Name the blood parasite species.
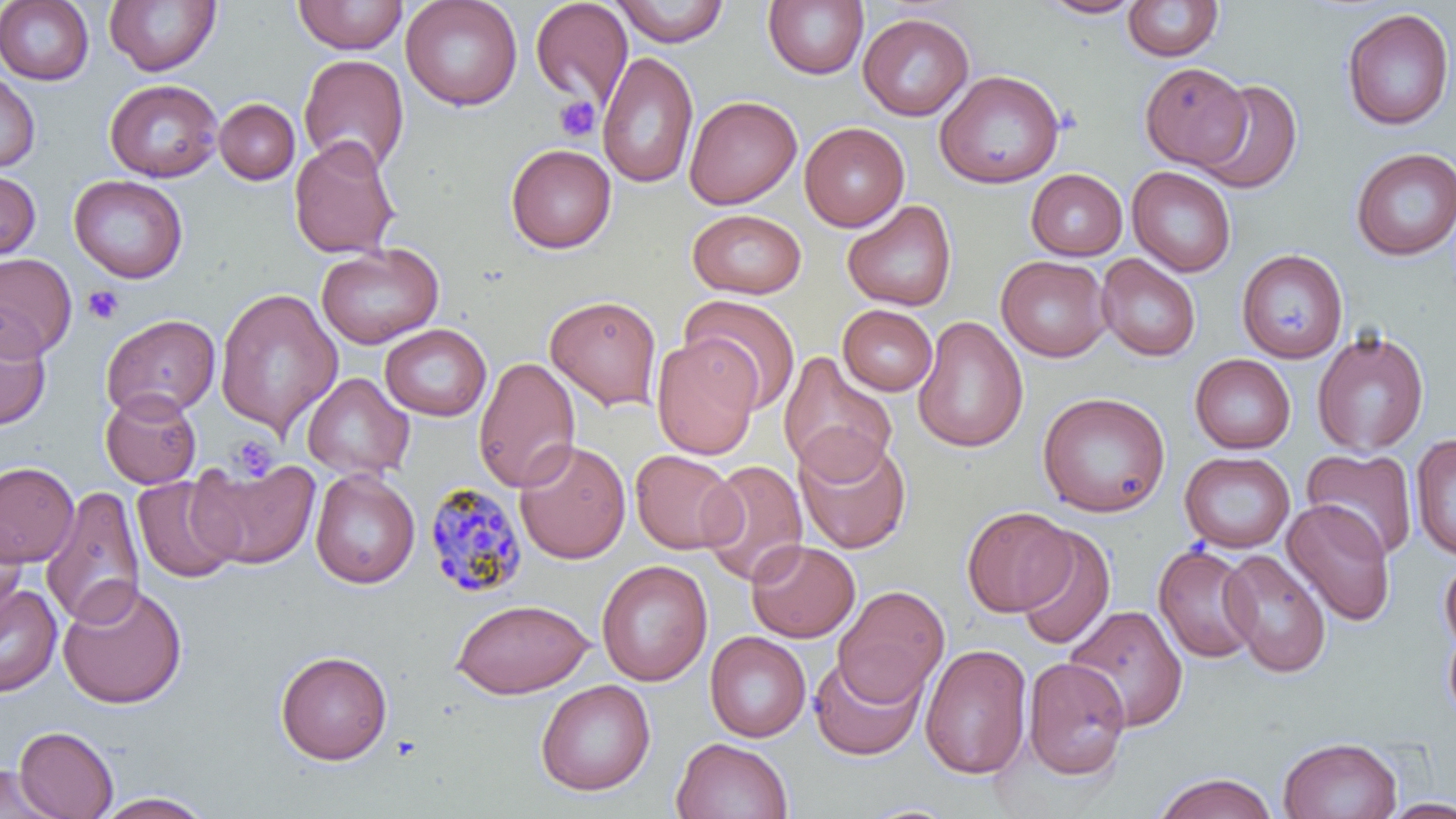
Plasmodium malariae.

Approximate bounding boxes as (x1,y1)-(x2,y2) corner pairs in pixels. Plasmodium malariae-infected red blood cell locations: (423,482)-(530,599). Platelet locations: (554,96)-(601,143), (82,285)-(124,326), (228,434)-(279,481). Uninfected red blood cell locations: (0,0)-(94,85), (292,0)-(409,54), (401,0)-(523,111), (530,0)-(633,108), (611,0)-(730,47), (1035,0)-(1146,19), (104,1)-(222,76), (763,1)-(869,80), (1122,1)-(1222,62), (1340,8)-(1454,131), (858,12)-(974,120), (597,51)-(699,188), (298,54)-(410,174), (1140,62)-(1251,168), (935,69)-(1065,189), (0,70)-(40,172), (104,79)-(222,182), (1196,79)-(1303,194), (684,95)-(802,209), (214,99)-(299,185), (799,123)-(909,231), (288,135)-(401,259), (505,144)-(617,253), (1351,148)-(1456,260), (1127,165)-(1236,277), (0,168)-(40,262), (1026,169)-(1127,260), (69,174)-(187,283), (841,199)-(957,312), (687,209)-(807,299), (316,243)-(443,349), (1236,249)-(1348,363), (0,253)-(77,360), (1096,253)-(1201,362), (996,255)-(1111,362), (215,288)-(341,435), (545,294)-(662,410), (681,295)-(802,412), (837,304)-(938,396), (101,313)-(220,420), (0,315)-(52,431), (912,316)-(1028,454), (380,324)-(492,420), (1312,329)-(1430,456), (651,335)-(761,460), (777,351)-(898,481), (1189,353)-(1296,454), (473,356)-(580,492), (301,372)-(415,482), (101,389)-(202,488), (1036,391)-(1171,518), (793,432)-(911,555), (1410,435)-(1456,560), (514,439)-(631,564), (1302,447)-(1419,561), (630,449)-(742,554), (1180,451)-(1295,553), (189,457)-(321,569), (697,460)-(808,586), (0,461)-(79,567), (310,468)-(420,589), (132,476)-(241,583), (41,486)-(145,629), (1282,499)-(1396,626), (961,506)-(1076,617), (0,515)-(26,624), (1014,525)-(1116,651), (746,539)-(860,643), (1152,543)-(1261,664), (1220,549)-(1332,678), (1439,552)-(1456,656), (596,559)-(713,687), (57,580)-(188,710), (0,583)-(62,697), (833,585)-(950,705), (452,598)-(594,699), (1064,604)-(1188,732), (1441,614)-(1456,730), (705,631)-(811,742), (920,644)-(1032,780), (275,649)-(393,765), (809,653)-(926,760), (1023,657)-(1131,780), (536,679)-(656,796), (14,725)-(118,819), (671,736)-(794,819), (1278,736)-(1402,819), (0,765)-(61,818), (1154,772)-(1277,819), (93,791)-(215,818), (1379,798)-(1456,818). May-Grünwald-Giemsa-stained preparation. 1000x magnification. Light microscopy. Thin blood film. One field of a larger specimen. Image is 1456×819 pixels.